Assess this cell for malaria.
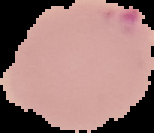

It is parasitized.

Summary:
  - Image size: 154×133 pixels
  - Preparation: thin blood smear
  - Image type: segmented cell region with the area outside set to black